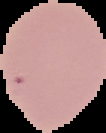

Summary:
  - Result: no Plasmodium parasites detected
  - Image type: segmented cell region on a black background
  - Preparation: thin blood film
  - Image size: 106×133 pixels